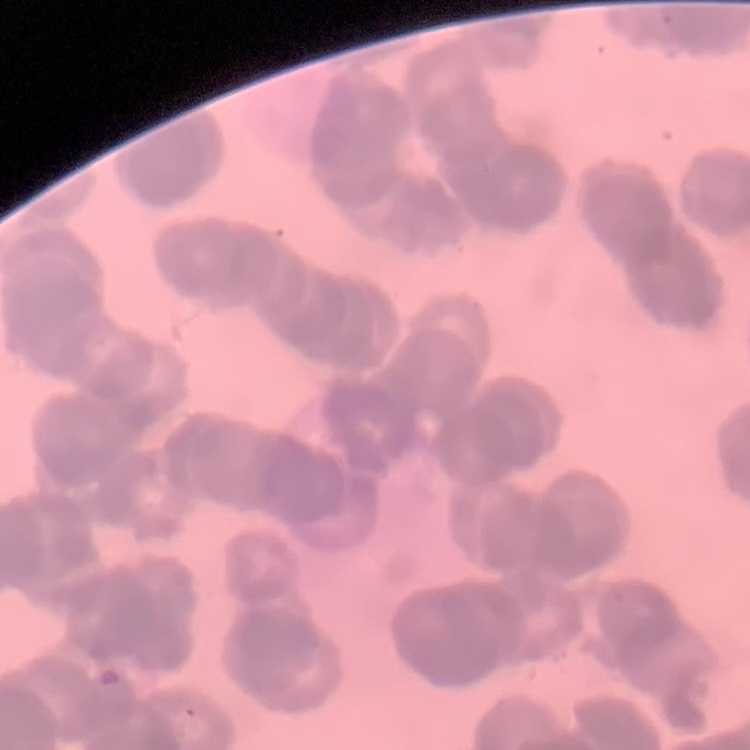 The erythrocytes exhibit rouleaux formation. Stained with either Field's or Giemsa. Thin peripheral smear. One tile cut from a larger photomicrograph.